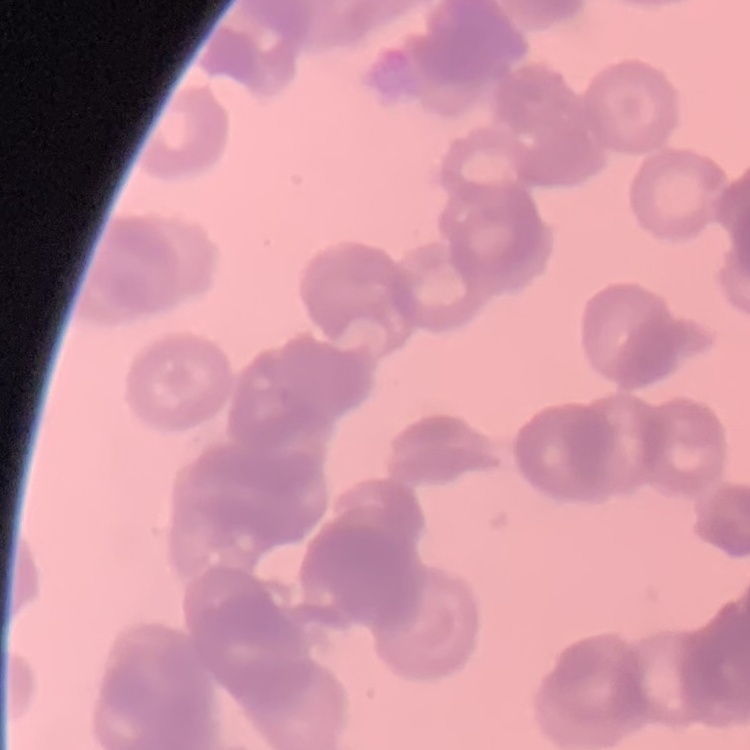
erythrocyte_morphology: rouleaux formation
preparation: thin blood smear
stain: Field's or Giemsa
image_type: one tile cut from a larger photomicrograph